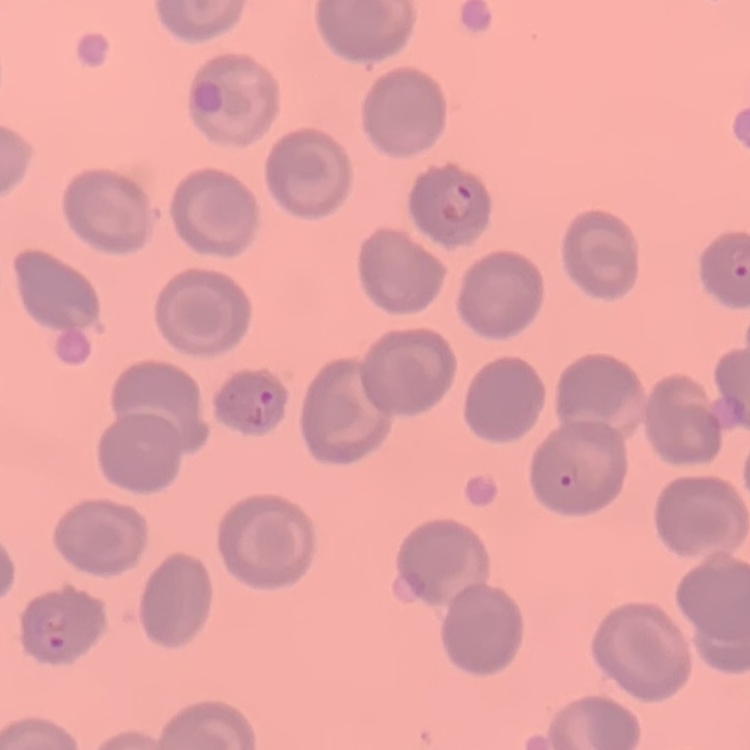

The erythrocytes exhibit no rouleaux formation. Stained with either Field's or Giemsa. Thin peripheral smear. One tile cut from a larger photomicrograph.